Locate and identify every blood parasite.
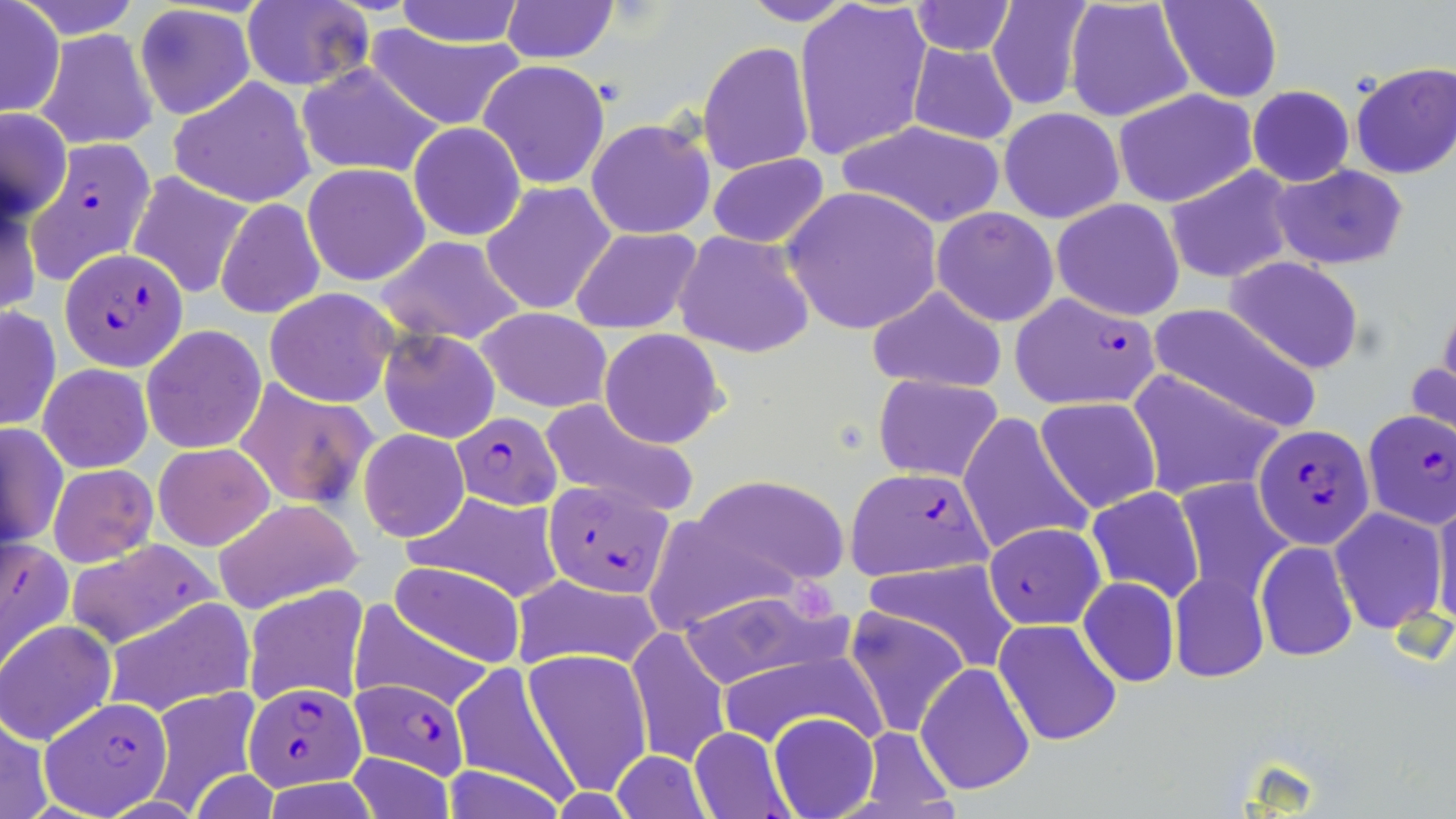
Approximate bounding boxes as (x1, y1, x2, y2) in pixels.
Plasmodium falciparum-infected red blood cells: (31, 138, 155, 278), (60, 247, 187, 371), (1010, 291, 1162, 409), (1362, 409, 1456, 529), (451, 413, 562, 511), (1254, 424, 1372, 546), (843, 467, 995, 581), (544, 478, 675, 596), (983, 523, 1106, 630), (1, 533, 74, 677), (61, 540, 220, 648), (349, 677, 469, 778), (245, 680, 367, 790), (42, 696, 174, 814).
No Plasmodium ovale, Plasmodium malariae, Plasmodium vivax, Babesia divergens, or Trypanosoma brucei observed.

{
  "slide_level_diagnosis": "Plasmodium falciparum",
  "preparation": "thin blood smear",
  "magnification": "1000x",
  "platelet_locations": "approximate bounding boxes as (x1, y1, x2, y2) in pixels: (791, 580, 837, 628)",
  "stain": "May-Grünwald-Giemsa",
  "field_of_view": "single",
  "uninfected_red_blood_cell_locations": "approximate bounding boxes as (x1, y1, x2, y2) in pixels: (8, 0, 147, 39), (736, 0, 858, 26), (792, 0, 933, 162), (1159, 0, 1281, 103), (241, 1, 373, 89), (391, 1, 528, 47), (499, 1, 619, 64), (908, 1, 1015, 55), (984, 1, 1093, 109), (1064, 1, 1195, 124), (1, 2, 63, 118), (134, 4, 255, 121), (38, 29, 158, 149), (364, 29, 526, 130), (697, 41, 815, 176), (907, 41, 1020, 146), (1073, 49, 1215, 185), (479, 60, 610, 189), (296, 62, 443, 179), (1351, 63, 1456, 178), (168, 77, 318, 207), (1248, 86, 1354, 187), (1113, 90, 1259, 208), (999, 106, 1125, 225), (1, 108, 72, 219), (586, 117, 716, 239), (834, 121, 1008, 228), (408, 122, 526, 241), (706, 153, 830, 250), (303, 164, 430, 286), (1164, 164, 1295, 285), (1269, 164, 1407, 269), (126, 170, 253, 300), (0, 182, 42, 319), (482, 182, 616, 316), (782, 186, 944, 336), (215, 196, 325, 319), (1051, 199, 1186, 320), (931, 206, 1059, 326), (571, 227, 703, 335), (674, 230, 813, 358), (373, 235, 529, 346), (1225, 256, 1365, 373), (866, 285, 1008, 392), (263, 287, 403, 406), (1146, 302, 1323, 436), (0, 305, 60, 431), (476, 306, 614, 413), (141, 325, 267, 454), (378, 329, 500, 443), (598, 329, 727, 447), (1407, 351, 1455, 451), (38, 363, 153, 472), (1128, 369, 1287, 500), (872, 373, 1004, 481), (233, 377, 376, 510), (1035, 396, 1162, 513), (539, 397, 699, 517), (956, 411, 1093, 556), (2, 422, 66, 549), (358, 429, 469, 541), (153, 442, 275, 550), (49, 465, 156, 567), (693, 474, 850, 589), (1172, 477, 1295, 604), (1087, 486, 1203, 604), (1432, 491, 1456, 631), (405, 492, 565, 603), (209, 497, 361, 615), (1329, 507, 1447, 635), (641, 523, 803, 629), (1255, 540, 1359, 663), (857, 559, 1018, 672), (388, 561, 526, 666), (1169, 570, 1269, 683), (507, 572, 670, 671), (1078, 577, 1180, 688), (244, 585, 369, 709), (674, 585, 853, 689), (100, 597, 252, 716), (348, 601, 494, 712), (842, 607, 970, 738), (994, 619, 1123, 747), (1, 622, 115, 744), (626, 626, 729, 769), (709, 645, 882, 747), (525, 648, 651, 795), (449, 659, 581, 802), (915, 661, 1036, 796), (143, 687, 264, 811), (0, 712, 52, 819), (769, 712, 879, 819), (689, 728, 791, 817), (342, 752, 457, 819), (608, 752, 714, 819), (191, 771, 282, 819)",
  "modality": "light microscopy",
  "image_size": "1456×819 pixels"
}